Report the malaria status of this cell.
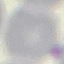
It is uninfected.

Summary:
  - Capture: smartphone through the microscope eyepiece
  - Stain: Giemsa
  - Image type: automatically extracted cell patch, resized to 64 × 64 pixels
  - Preparation: thin blood film